Outline platelets.
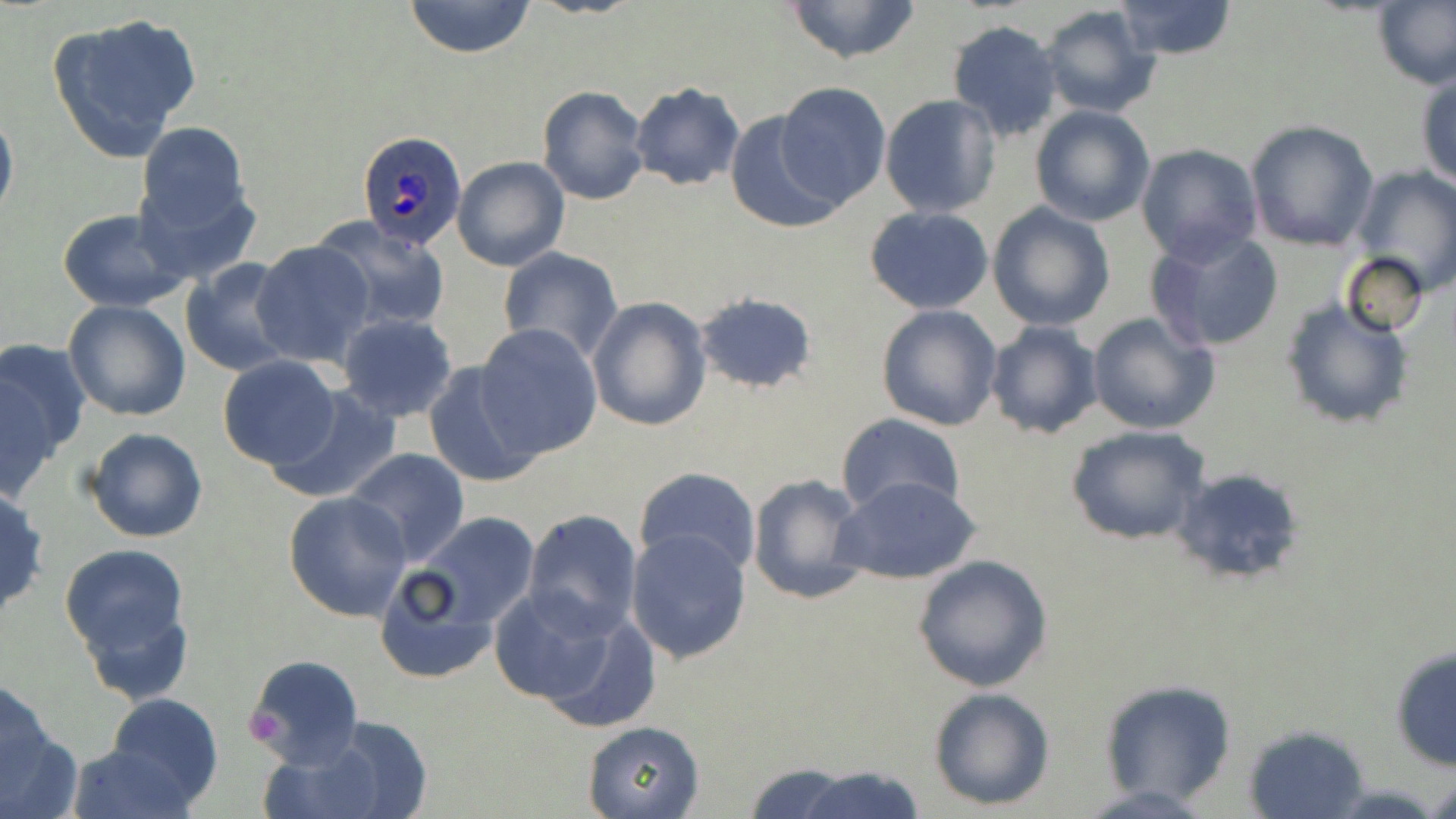
Approximate bounding boxes as [x1, y1, x2, y2] in pixels.
Platelets: [239, 700, 293, 748].

Summary:
  - Uninfected red blood cell locations: [403, 0, 537, 58], [780, 0, 926, 66], [1113, 0, 1238, 61], [1373, 1, 1456, 91], [1039, 5, 1162, 116], [48, 10, 202, 161], [946, 20, 1063, 142], [1416, 69, 1456, 190], [628, 82, 744, 192], [775, 82, 891, 208], [537, 85, 649, 205], [879, 94, 1002, 219], [1029, 104, 1156, 227], [0, 105, 18, 230], [723, 110, 847, 232], [1245, 120, 1379, 252], [134, 121, 254, 247], [1134, 144, 1262, 265], [452, 156, 570, 272], [1353, 165, 1456, 297], [987, 201, 1116, 333], [864, 206, 994, 313], [57, 208, 190, 311], [317, 220, 449, 330], [1146, 228, 1284, 354], [252, 239, 375, 366], [498, 246, 623, 364], [1340, 252, 1430, 337], [180, 259, 298, 378], [693, 289, 817, 394], [587, 296, 711, 432], [1279, 297, 1414, 432], [63, 299, 192, 421], [875, 304, 1004, 431], [1087, 309, 1220, 436], [336, 312, 459, 422], [985, 321, 1103, 439], [472, 324, 603, 458], [0, 338, 88, 492], [217, 356, 341, 470], [421, 361, 544, 487], [265, 382, 403, 505], [834, 413, 966, 521], [1065, 424, 1213, 547], [82, 426, 209, 544], [344, 448, 470, 566], [633, 465, 762, 578], [1168, 465, 1309, 587], [747, 471, 871, 605], [834, 475, 983, 588], [0, 482, 50, 623], [284, 491, 413, 622], [400, 508, 544, 644], [522, 508, 644, 636], [624, 527, 752, 665], [60, 543, 192, 688], [374, 551, 521, 683], [912, 554, 1054, 691], [490, 585, 629, 712], [538, 606, 663, 734], [1388, 645, 1455, 772], [246, 652, 363, 769], [1098, 678, 1238, 806], [927, 686, 1056, 811], [0, 688, 81, 819], [104, 690, 224, 810], [298, 718, 435, 819], [581, 719, 706, 818], [1240, 722, 1371, 819], [65, 742, 197, 818], [742, 762, 863, 818], [788, 764, 927, 819], [1425, 776, 1455, 818]
  - Plasmodium ovale-infected red blood cell locations: [356, 131, 464, 254]
  - Slide-level diagnosis: Plasmodium ovale
  - Preparation: thin blood film
  - Field of view: single
  - Modality: light microscopy
  - Image size: 1456×819 pixels
  - Magnification: 1000x
  - Stain: May-Grünwald-Giemsa